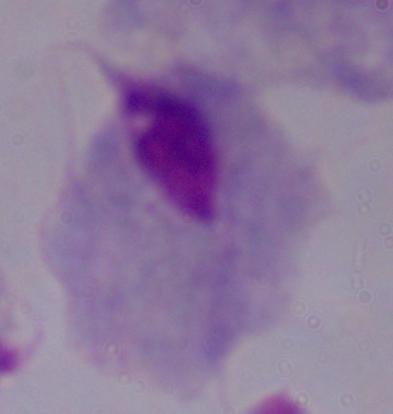
identification: trichomonad
magnification: 1000x
modality: photomicrograph